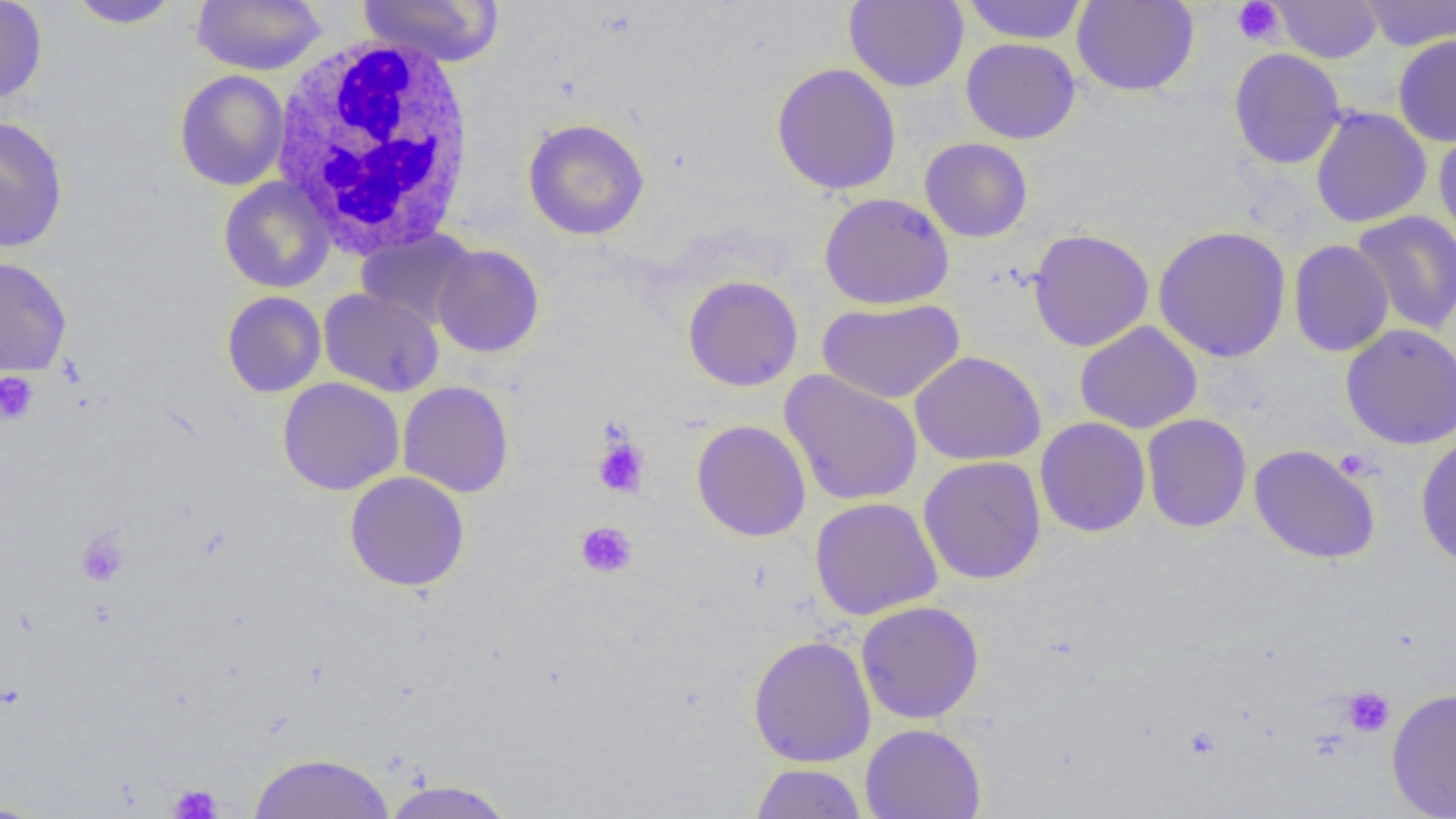

Summary:
  - Coordinate format: approximate bounding boxes as [x1, y1, x2, y2] in pixels
  - Platelet locations: [1231, 0, 1285, 47], [0, 372, 38, 425], [592, 435, 650, 498], [1334, 448, 1377, 481], [575, 522, 637, 578], [76, 530, 130, 587], [1339, 686, 1395, 737], [168, 783, 223, 819]
  - Uninfected red blood cell locations: [0, 0, 48, 104], [191, 0, 325, 75], [356, 0, 504, 67], [844, 0, 968, 92], [961, 0, 1089, 45], [1071, 0, 1199, 96], [1358, 0, 1456, 51], [68, 1, 182, 29], [1272, 1, 1382, 63], [1393, 35, 1456, 147], [961, 38, 1081, 144], [1229, 48, 1346, 169], [771, 63, 902, 196], [174, 69, 290, 191], [1310, 107, 1431, 228], [0, 116, 69, 253], [522, 118, 650, 241], [1433, 123, 1456, 246], [919, 138, 1033, 243], [218, 176, 336, 293], [819, 192, 955, 310], [1351, 210, 1456, 336], [1153, 225, 1292, 363], [1028, 228, 1154, 352], [356, 229, 477, 330], [1289, 239, 1394, 357], [431, 243, 545, 358], [0, 255, 72, 377], [683, 275, 803, 392], [318, 287, 444, 397], [222, 291, 326, 397], [817, 298, 964, 405], [1074, 321, 1203, 434], [1341, 323, 1456, 450], [909, 351, 1046, 466], [779, 370, 924, 506], [277, 377, 405, 496], [398, 381, 514, 498], [1142, 413, 1252, 532], [1035, 417, 1151, 537], [692, 420, 811, 542], [1415, 434, 1456, 570], [1248, 444, 1381, 565], [918, 455, 1046, 585], [344, 471, 470, 592], [810, 496, 943, 620], [856, 600, 984, 724], [748, 635, 876, 767], [1387, 687, 1456, 818], [860, 723, 986, 819], [248, 752, 396, 818], [749, 763, 867, 819], [381, 779, 517, 819], [0, 800, 54, 818]
  - White blood cell locations: [269, 34, 480, 256]
  - Slide-level diagnosis: negative for blood parasites
  - Image size: 1456×819 pixels
  - Field of view: single
  - Magnification: 1000x
  - Modality: light microscopy
  - Preparation: thin blood film